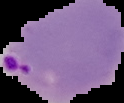 Malaria status: parasitized. The area outside the segmented cell region is set to black. Image is 124×103 pixels. From a thin blood film.